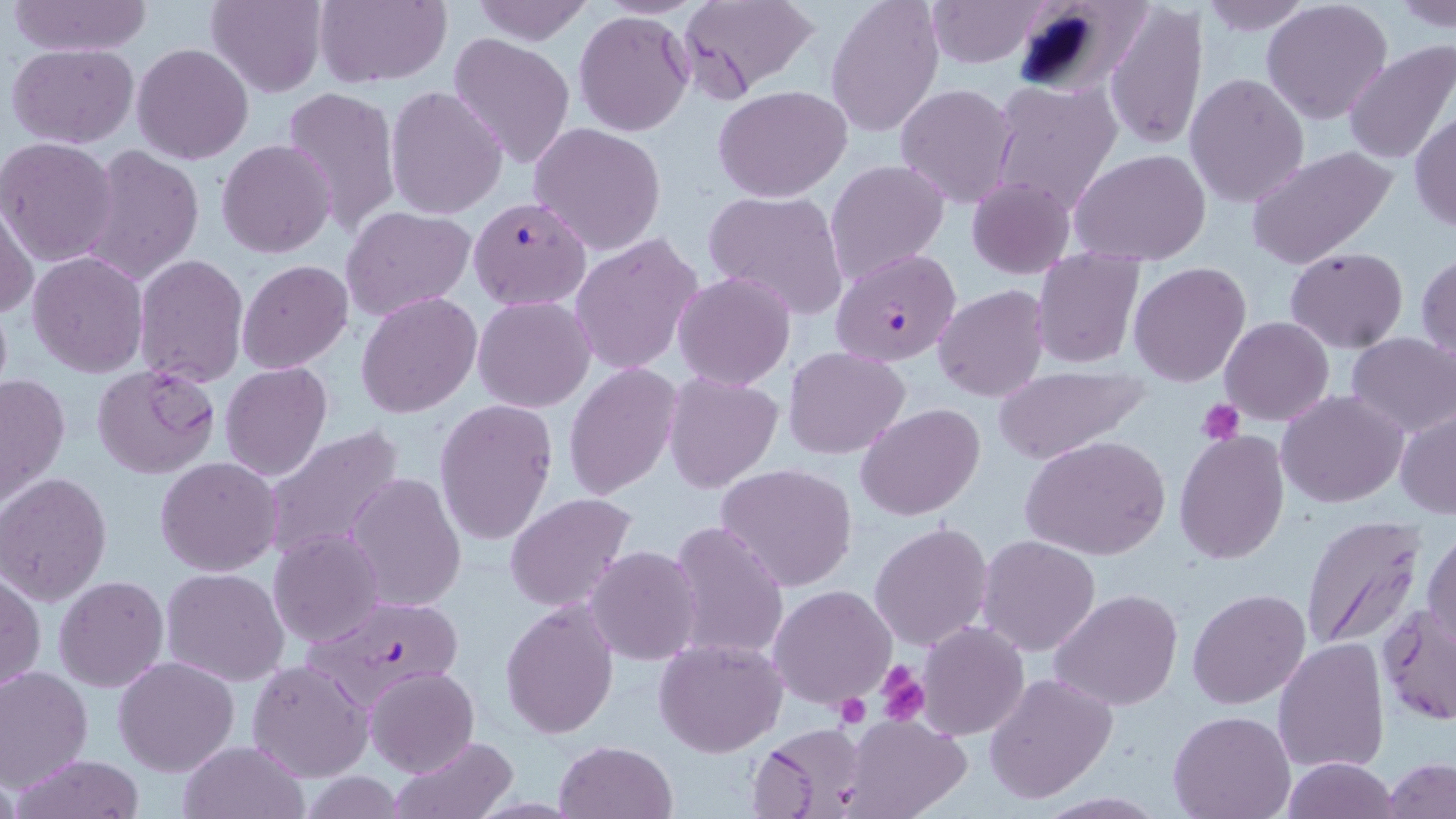
Summary:
  - Coordinate format: approximate bounding boxes as named x1/y1/x2/y2 corners in pixels
  - Uninfected red blood cell locations: (x1=7, y1=0, x2=153, y2=56), (x1=207, y1=0, x2=326, y2=96), (x1=312, y1=0, x2=451, y2=88), (x1=681, y1=0, x2=821, y2=97), (x1=825, y1=0, x2=943, y2=139), (x1=925, y1=0, x2=1052, y2=67), (x1=1011, y1=0, x2=1144, y2=100), (x1=1196, y1=0, x2=1315, y2=36), (x1=1262, y1=0, x2=1394, y2=124), (x1=467, y1=1, x2=597, y2=44), (x1=1391, y1=1, x2=1456, y2=30), (x1=1106, y1=2, x2=1206, y2=151), (x1=575, y1=10, x2=693, y2=137), (x1=448, y1=34, x2=577, y2=169), (x1=1343, y1=41, x2=1456, y2=164), (x1=6, y1=43, x2=140, y2=148), (x1=132, y1=43, x2=254, y2=165), (x1=1184, y1=74, x2=1310, y2=208), (x1=987, y1=80, x2=1123, y2=217), (x1=895, y1=83, x2=1019, y2=207), (x1=385, y1=85, x2=509, y2=218), (x1=280, y1=86, x2=401, y2=233), (x1=715, y1=86, x2=851, y2=201), (x1=1410, y1=110, x2=1456, y2=233), (x1=528, y1=122, x2=666, y2=255), (x1=1, y1=137, x2=121, y2=267), (x1=216, y1=139, x2=338, y2=258), (x1=76, y1=145, x2=204, y2=288), (x1=1244, y1=145, x2=1400, y2=270), (x1=1070, y1=149, x2=1212, y2=265), (x1=824, y1=157, x2=948, y2=288), (x1=966, y1=176, x2=1075, y2=279), (x1=704, y1=189, x2=850, y2=320), (x1=1, y1=197, x2=38, y2=321), (x1=341, y1=204, x2=477, y2=319), (x1=570, y1=233, x2=704, y2=376), (x1=1286, y1=247, x2=1407, y2=353), (x1=832, y1=248, x2=963, y2=368), (x1=1032, y1=249, x2=1144, y2=370), (x1=27, y1=251, x2=149, y2=377), (x1=1417, y1=253, x2=1456, y2=361), (x1=133, y1=254, x2=249, y2=390), (x1=236, y1=260, x2=354, y2=374), (x1=1129, y1=262, x2=1252, y2=386), (x1=673, y1=271, x2=796, y2=390), (x1=933, y1=283, x2=1051, y2=402), (x1=356, y1=293, x2=483, y2=418), (x1=474, y1=296, x2=595, y2=412), (x1=1221, y1=316, x2=1334, y2=425), (x1=1345, y1=333, x2=1456, y2=439), (x1=783, y1=345, x2=909, y2=459), (x1=90, y1=362, x2=220, y2=479), (x1=220, y1=363, x2=333, y2=481), (x1=564, y1=363, x2=683, y2=501), (x1=990, y1=365, x2=1146, y2=462), (x1=663, y1=372, x2=783, y2=493), (x1=0, y1=373, x2=69, y2=504), (x1=1276, y1=390, x2=1408, y2=509), (x1=435, y1=399, x2=559, y2=547), (x1=855, y1=403, x2=986, y2=519), (x1=1395, y1=409, x2=1456, y2=519), (x1=260, y1=425, x2=406, y2=562), (x1=1174, y1=430, x2=1289, y2=562), (x1=1020, y1=435, x2=1172, y2=559), (x1=155, y1=457, x2=282, y2=576), (x1=716, y1=462, x2=859, y2=592), (x1=0, y1=473, x2=112, y2=604), (x1=347, y1=473, x2=467, y2=613), (x1=505, y1=493, x2=637, y2=613), (x1=1299, y1=516, x2=1427, y2=652), (x1=666, y1=520, x2=790, y2=664), (x1=869, y1=521, x2=995, y2=652), (x1=1425, y1=526, x2=1456, y2=651), (x1=268, y1=528, x2=385, y2=648), (x1=977, y1=535, x2=1102, y2=657), (x1=587, y1=546, x2=702, y2=665), (x1=160, y1=566, x2=291, y2=685), (x1=1, y1=572, x2=44, y2=696), (x1=54, y1=575, x2=169, y2=693), (x1=769, y1=584, x2=896, y2=710), (x1=1052, y1=589, x2=1183, y2=711), (x1=1188, y1=589, x2=1311, y2=710), (x1=500, y1=599, x2=619, y2=737), (x1=1379, y1=603, x2=1454, y2=725), (x1=916, y1=621, x2=1029, y2=739), (x1=654, y1=637, x2=786, y2=756), (x1=1274, y1=638, x2=1390, y2=774), (x1=113, y1=655, x2=240, y2=775), (x1=246, y1=659, x2=372, y2=782), (x1=0, y1=666, x2=93, y2=792), (x1=365, y1=667, x2=479, y2=778), (x1=984, y1=672, x2=1116, y2=805), (x1=1168, y1=711, x2=1294, y2=819), (x1=838, y1=714, x2=972, y2=819), (x1=748, y1=722, x2=871, y2=818), (x1=390, y1=734, x2=518, y2=818), (x1=178, y1=739, x2=308, y2=819), (x1=554, y1=740, x2=678, y2=819), (x1=10, y1=755, x2=146, y2=819), (x1=1280, y1=757, x2=1401, y2=818), (x1=1383, y1=760, x2=1456, y2=818), (x1=1034, y1=792, x2=1169, y2=818)
  - Plasmodium falciparum-infected red blood cell locations: (x1=470, y1=197, x2=590, y2=310), (x1=299, y1=595, x2=468, y2=710)
  - Platelet locations: (x1=1199, y1=401, x2=1244, y2=445), (x1=876, y1=662, x2=928, y2=723), (x1=833, y1=693, x2=870, y2=728)
  - Slide-level diagnosis: Plasmodium falciparum
  - Magnification: 1000x
  - Field of view: one of a larger specimen
  - Preparation: thin blood film
  - Modality: optical microscopy
  - Image size: 1456×819 pixels
  - Stain: May-Grünwald-Giemsa